Report the malaria status of this cell.
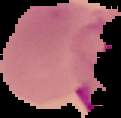

Parasitized.

Summary:
  - Image size: 121×118 pixels
  - Image type: segmented cell region with the area outside set to black
  - Preparation: thin blood smear